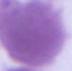 An erythrocyte is shown. 1000x magnification. Micrograph.